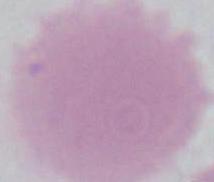

Summary:
  - Identification: red blood cell
  - Magnification: 1000x
  - Modality: photomicrograph